State which parasite is depicted.
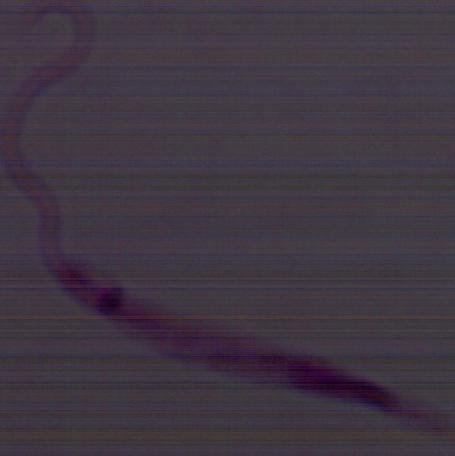

This is Leishmania.

Summary:
  - Modality: micrograph
  - Magnification: 1000x